Assess this cell for malaria.
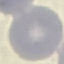

It is uninfected.

capture = smartphone camera at the microscope eyepiece
stain = Giemsa
preparation = thin blood film
image type = automatically extracted cell patch, resized to 64 × 64 pixels